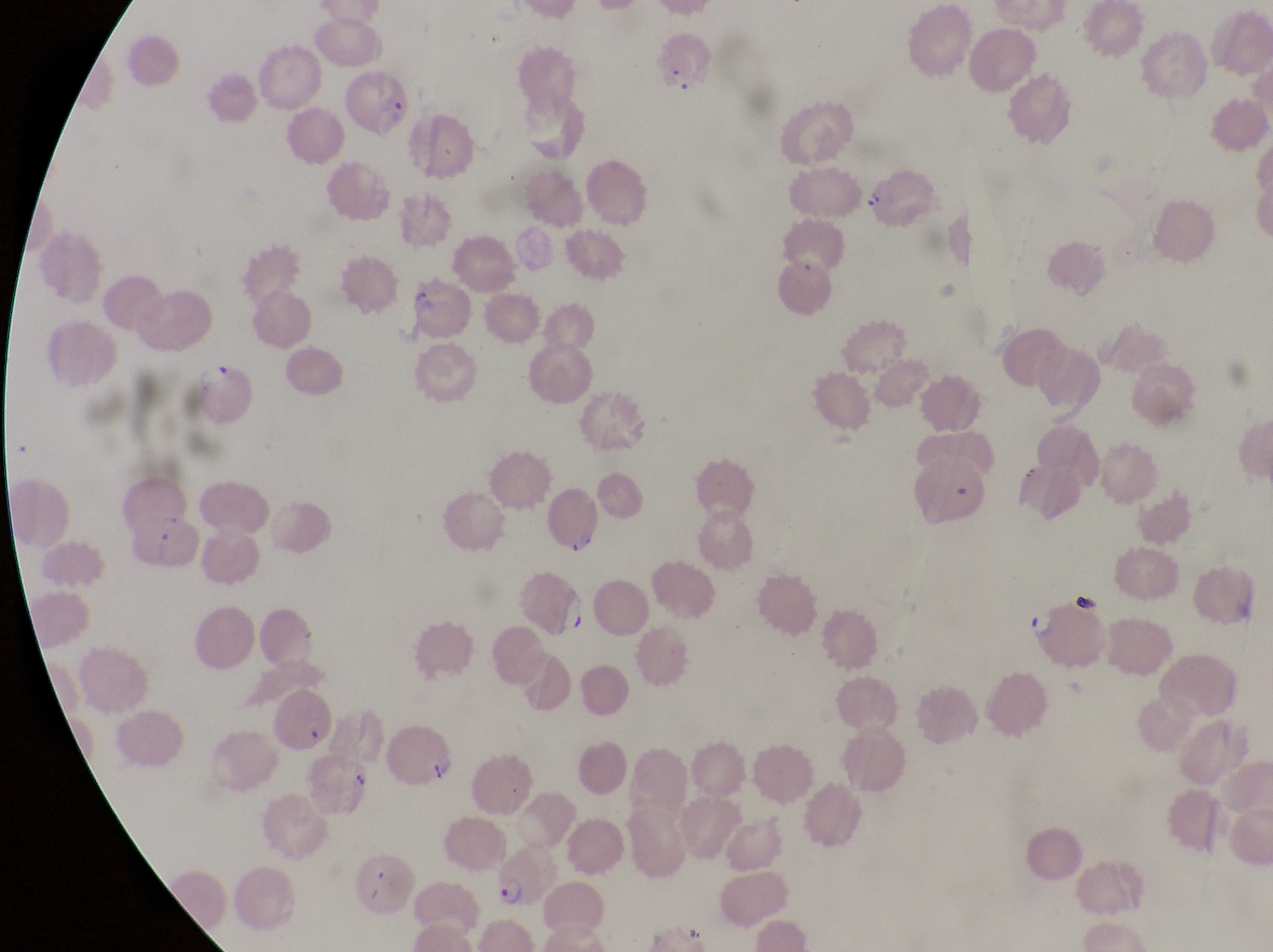 Approximate bounding boxes as (left, top, right, bottom) in pixels. Parasitised red blood cell locations: (651, 28, 711, 93), (347, 69, 416, 139), (869, 169, 940, 234), (409, 272, 472, 337), (197, 362, 263, 427), (548, 493, 603, 559), (130, 512, 204, 582), (1019, 594, 1112, 674), (385, 727, 465, 797), (500, 846, 557, 909), (359, 858, 414, 920). Photographed through the eyepiece of an Olympus CX-23 microscope with a smartphone camera. Image is 1273×952 pixels. One field of view. Magnification of 1000x. Sample from Uganda. Thin blood film.